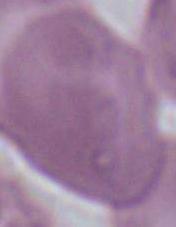
Summary:
  - Modality: micrograph
  - Magnification: 1000x
  - Identification: red blood cell